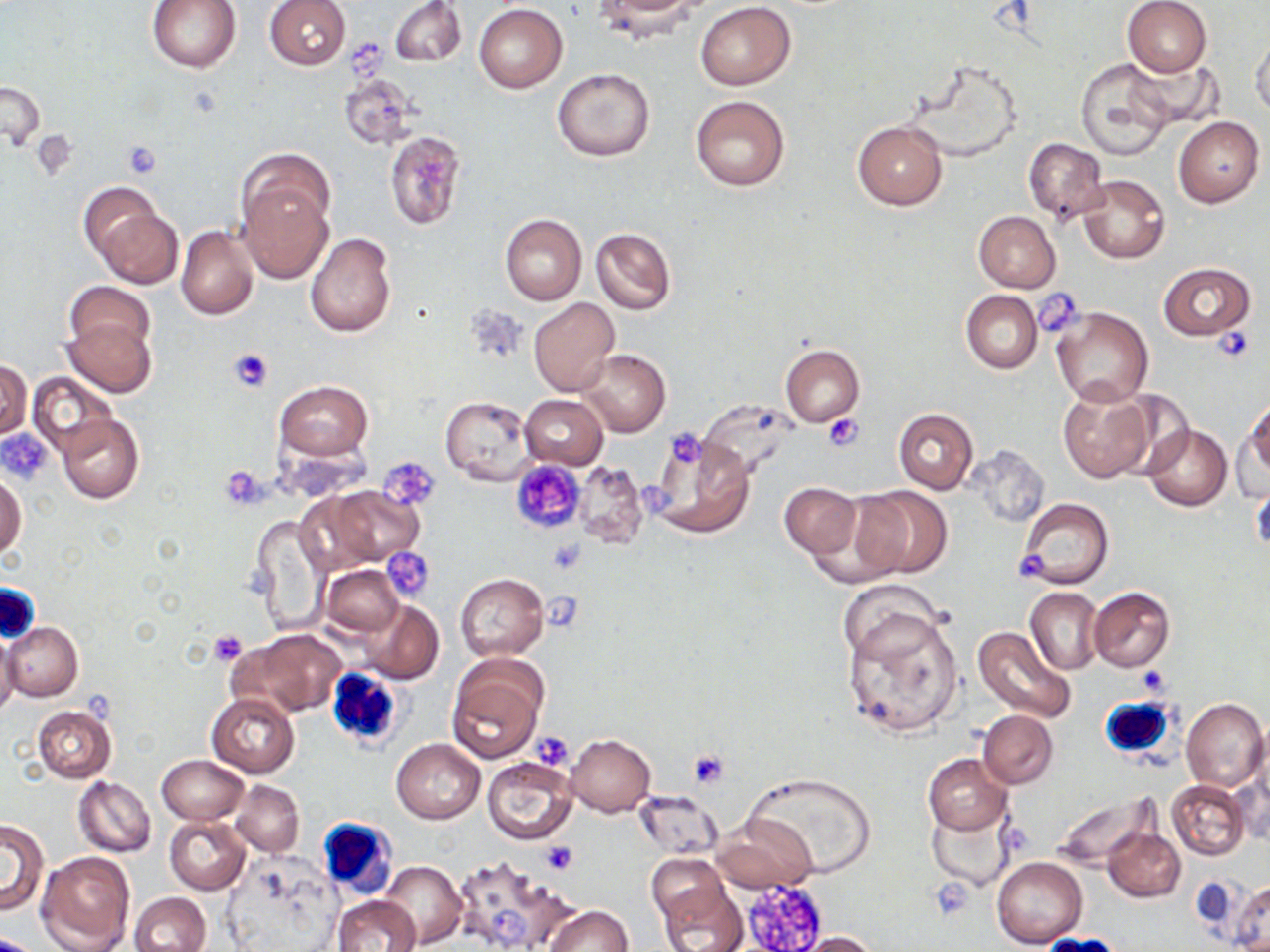

slide_level_diagnosis: no evidence of blood parasites
uninfected_red_blood_cell_locations: 'approximate bounding boxes as [x1, y1, x2, y2] in pixels: [148, 0, 240, 73], [264, 0, 351, 70], [390, 0, 464, 67], [1121, 0, 1212, 77], [591, 2, 701, 43], [697, 2, 796, 90], [474, 4, 568, 93], [1250, 35, 1270, 119], [1122, 56, 1221, 133], [1075, 58, 1177, 160], [552, 68, 655, 161], [338, 74, 418, 151], [0, 80, 44, 152], [690, 96, 790, 191], [1174, 116, 1264, 207], [852, 119, 948, 209], [385, 130, 466, 230], [1024, 137, 1109, 221], [237, 150, 335, 240], [1077, 174, 1169, 264], [78, 180, 167, 265], [239, 185, 332, 282], [94, 206, 184, 289], [974, 210, 1062, 293], [500, 213, 587, 305], [499, 223, 669, 312], [176, 225, 259, 320], [590, 227, 675, 315], [305, 232, 396, 338], [1159, 262, 1254, 340], [66, 281, 154, 357], [961, 290, 1043, 373], [528, 297, 619, 396], [1052, 306, 1154, 408], [60, 316, 156, 397], [781, 344, 863, 427], [579, 349, 671, 438], [0, 359, 31, 442], [28, 372, 115, 457], [273, 379, 373, 461], [1056, 383, 1154, 483], [519, 394, 608, 469], [440, 395, 536, 484], [1244, 398, 1270, 480], [893, 408, 978, 494], [57, 412, 144, 503], [1232, 418, 1270, 502], [1141, 424, 1231, 512], [650, 435, 755, 540], [966, 445, 1050, 528], [574, 461, 647, 550], [0, 472, 26, 560], [1250, 479, 1269, 560], [779, 482, 861, 558], [328, 486, 425, 566], [851, 486, 951, 579], [1016, 497, 1114, 589], [252, 514, 330, 638], [322, 565, 403, 636], [456, 573, 548, 660], [1025, 587, 1102, 676], [1089, 588, 1174, 672], [357, 599, 444, 684], [843, 608, 964, 739], [2, 622, 83, 700], [235, 627, 347, 717], [973, 627, 1078, 724], [0, 633, 18, 720], [447, 654, 548, 763], [206, 693, 299, 777], [1181, 697, 1268, 793], [33, 706, 115, 782], [978, 710, 1058, 787], [566, 733, 655, 816], [392, 739, 485, 823], [923, 753, 1012, 834], [157, 754, 248, 825], [482, 756, 577, 845], [744, 772, 878, 878], [74, 776, 156, 857], [232, 780, 304, 857], [1167, 780, 1250, 860], [632, 790, 724, 860], [1049, 793, 1160, 873], [928, 808, 1014, 888], [715, 814, 819, 892], [164, 816, 249, 894], [1, 820, 47, 914], [1104, 826, 1185, 902], [36, 850, 136, 952], [453, 854, 571, 952], [646, 854, 730, 928], [991, 856, 1087, 949], [222, 860, 336, 952], [380, 860, 466, 947], [657, 879, 748, 952], [1230, 879, 1270, 951], [129, 892, 211, 952], [333, 896, 422, 952], [545, 904, 632, 952], [792, 931, 881, 951]'
preparation: thin blood film
magnification: 1000x
image_size: 1270×952 pixels
platelet_locations: 'approximate bounding boxes as [x1, y1, x2, y2] in pixels: [345, 38, 393, 77], [122, 139, 165, 178], [1035, 290, 1087, 336], [1211, 322, 1256, 364], [228, 349, 273, 393], [822, 413, 864, 449], [664, 427, 708, 471], [3, 432, 54, 482], [380, 457, 442, 511], [511, 460, 585, 533], [220, 469, 268, 508], [546, 540, 584, 574], [382, 547, 435, 602], [1009, 548, 1051, 584], [545, 594, 583, 632], [209, 629, 246, 665], [1137, 666, 1170, 696], [530, 731, 575, 770], [687, 749, 731, 790], [542, 842, 577, 874], [742, 877, 829, 951], [928, 879, 977, 920], [486, 904, 531, 946]'
white_blood_cell_locations: 'approximate bounding boxes as [x1, y1, x2, y2] in pixels: [0, 582, 41, 642], [324, 667, 405, 751], [1098, 695, 1175, 760], [316, 817, 399, 901]'
stain: May-Grünwald-Giemsa
modality: optical microscopy
field_of_view: one of a larger specimen